Name the cell type shown.
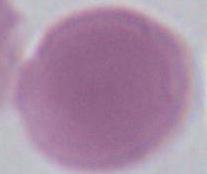

An erythrocyte.

modality = photomicrograph
magnification = 1000x